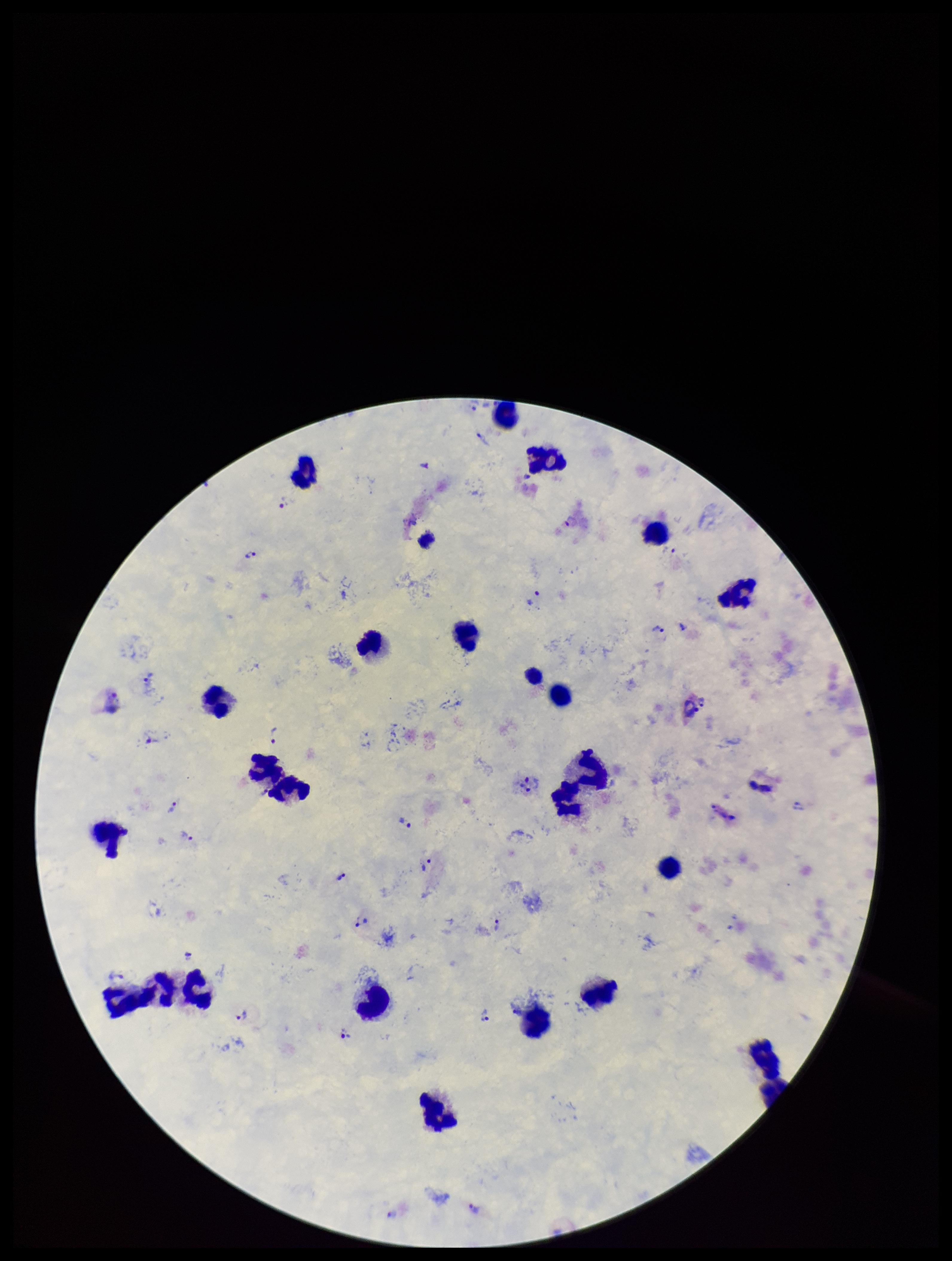
Parasite count: 28. Single field of view. Leukocyte count: 22. Preparation: thick. Stained with Giemsa. Species reported for this patient: Plasmodium vivax. Photographed through the microscope eyepiece with a smartphone camera. Plasmodium parasites: seen. Image is 952×1261 pixels. Patient malaria status: infected.